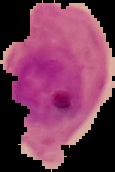

From a thin blood smear. Image is 115×172 pixels. Result: malaria parasites detected. Segmented cell region on a black background.